State which cell type is depicted.
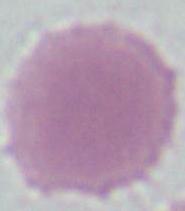

An erythrocyte.

Summary:
  - Magnification: 1000x
  - Modality: photomicrograph